Comment on the morphology of the erythrocytes.
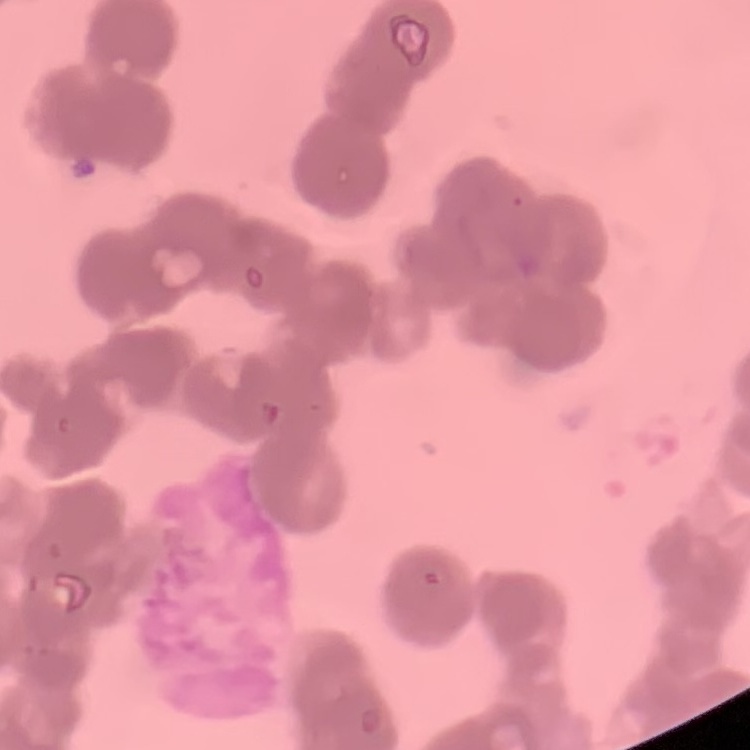
They show rouleaux formation.

Summary:
  - Image type: one tile cut from a larger photomicrograph
  - Stain: Field's or Giemsa
  - Preparation: thin blood smear